Assess this cell for malaria.
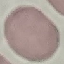

It is uninfected.

stain = Giemsa
image type = cell patch, automatically extracted from a larger field of view and resized to 64 × 64 pixels
capture = smartphone through the microscope eyepiece
preparation = thin blood film